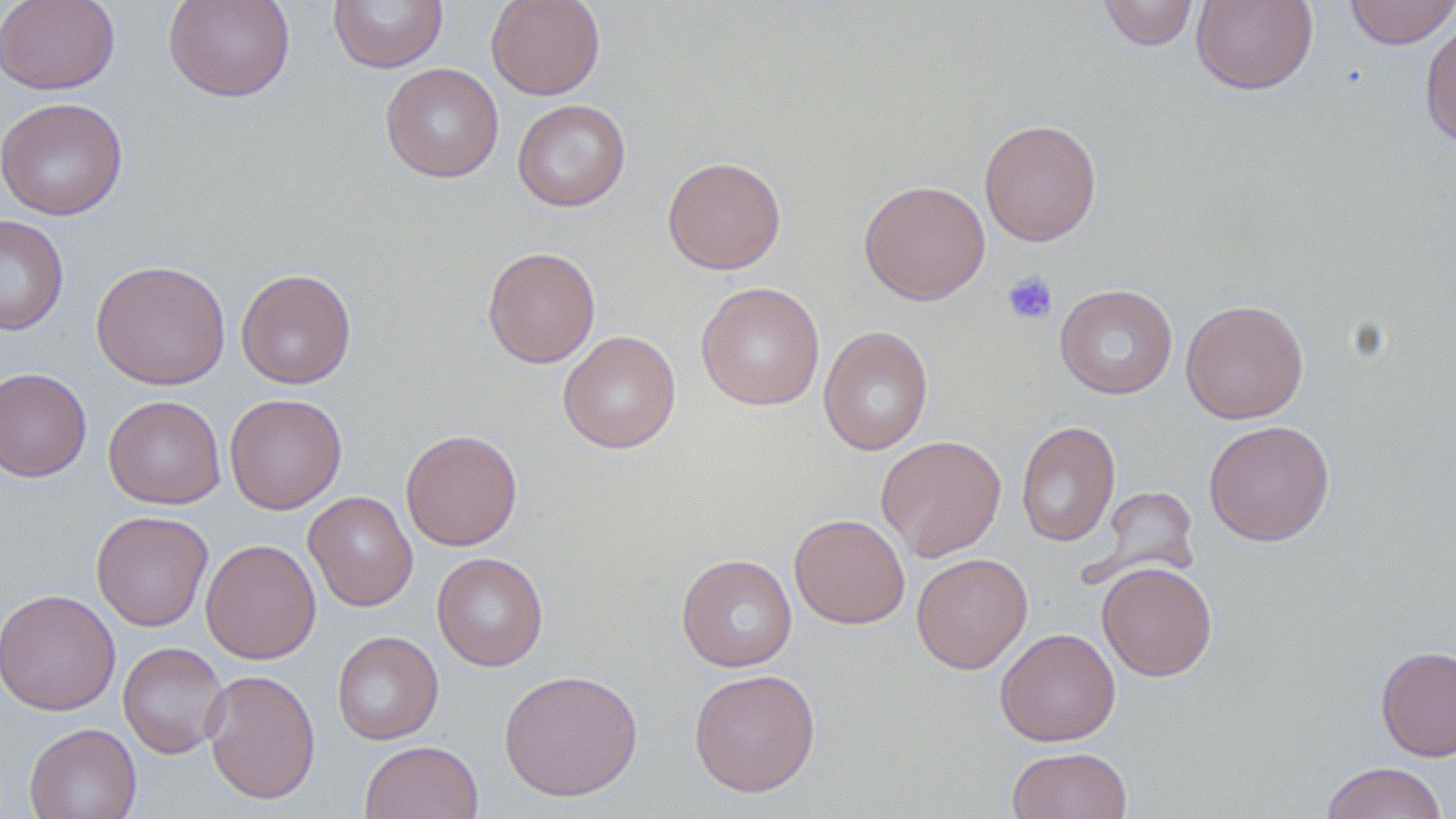
Summary:
  - Coordinate format: approximate bounding boxes as named x1/y1/x2/y2 corners in pixels
  - Platelet locations: (x1=1002, y1=270, x2=1058, y2=325)
  - Uninfected red blood cell locations: (x1=0, y1=0, x2=119, y2=95), (x1=163, y1=0, x2=296, y2=103), (x1=328, y1=0, x2=449, y2=73), (x1=486, y1=0, x2=605, y2=100), (x1=1098, y1=0, x2=1199, y2=50), (x1=1191, y1=0, x2=1319, y2=95), (x1=1343, y1=0, x2=1455, y2=49), (x1=1420, y1=17, x2=1456, y2=150), (x1=380, y1=62, x2=504, y2=183), (x1=0, y1=96, x2=128, y2=221), (x1=512, y1=99, x2=631, y2=212), (x1=979, y1=118, x2=1102, y2=247), (x1=662, y1=156, x2=786, y2=275), (x1=858, y1=179, x2=991, y2=305), (x1=0, y1=214, x2=69, y2=336), (x1=482, y1=246, x2=600, y2=368), (x1=91, y1=259, x2=231, y2=390), (x1=235, y1=268, x2=357, y2=389), (x1=696, y1=282, x2=825, y2=410), (x1=1055, y1=284, x2=1178, y2=399), (x1=1180, y1=299, x2=1309, y2=424), (x1=819, y1=325, x2=933, y2=456), (x1=558, y1=330, x2=680, y2=454), (x1=0, y1=367, x2=92, y2=482), (x1=103, y1=394, x2=226, y2=509), (x1=224, y1=394, x2=347, y2=514), (x1=1016, y1=420, x2=1120, y2=547), (x1=1204, y1=420, x2=1335, y2=546), (x1=401, y1=429, x2=523, y2=551), (x1=876, y1=435, x2=1007, y2=561), (x1=1091, y1=485, x2=1199, y2=585), (x1=304, y1=490, x2=418, y2=612), (x1=91, y1=510, x2=214, y2=631), (x1=790, y1=514, x2=910, y2=629), (x1=200, y1=538, x2=322, y2=664), (x1=432, y1=552, x2=548, y2=671), (x1=911, y1=552, x2=1033, y2=674), (x1=676, y1=553, x2=797, y2=672), (x1=1097, y1=560, x2=1217, y2=681), (x1=0, y1=588, x2=121, y2=716), (x1=995, y1=627, x2=1120, y2=746), (x1=332, y1=631, x2=443, y2=745), (x1=117, y1=641, x2=230, y2=759), (x1=1376, y1=645, x2=1456, y2=761), (x1=688, y1=667, x2=821, y2=797), (x1=499, y1=668, x2=644, y2=802), (x1=202, y1=669, x2=321, y2=805), (x1=24, y1=722, x2=141, y2=819), (x1=359, y1=740, x2=484, y2=819), (x1=1007, y1=746, x2=1133, y2=819), (x1=1320, y1=761, x2=1449, y2=819)
  - Slide-level diagnosis: no evidence of blood parasites
  - Magnification: 1000x
  - Field of view: single
  - Preparation: thin blood smear
  - Modality: light microscopy
  - Image size: 1456×819 pixels
  - Stain: May-Grünwald-Giemsa